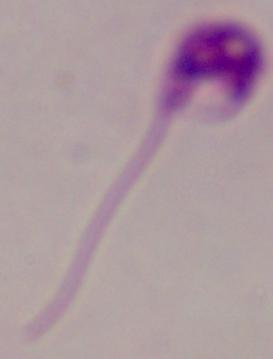

Summary:
  - Identification: Leishmania
  - Magnification: 1000x
  - Modality: photomicrograph